Name the blood parasite species.
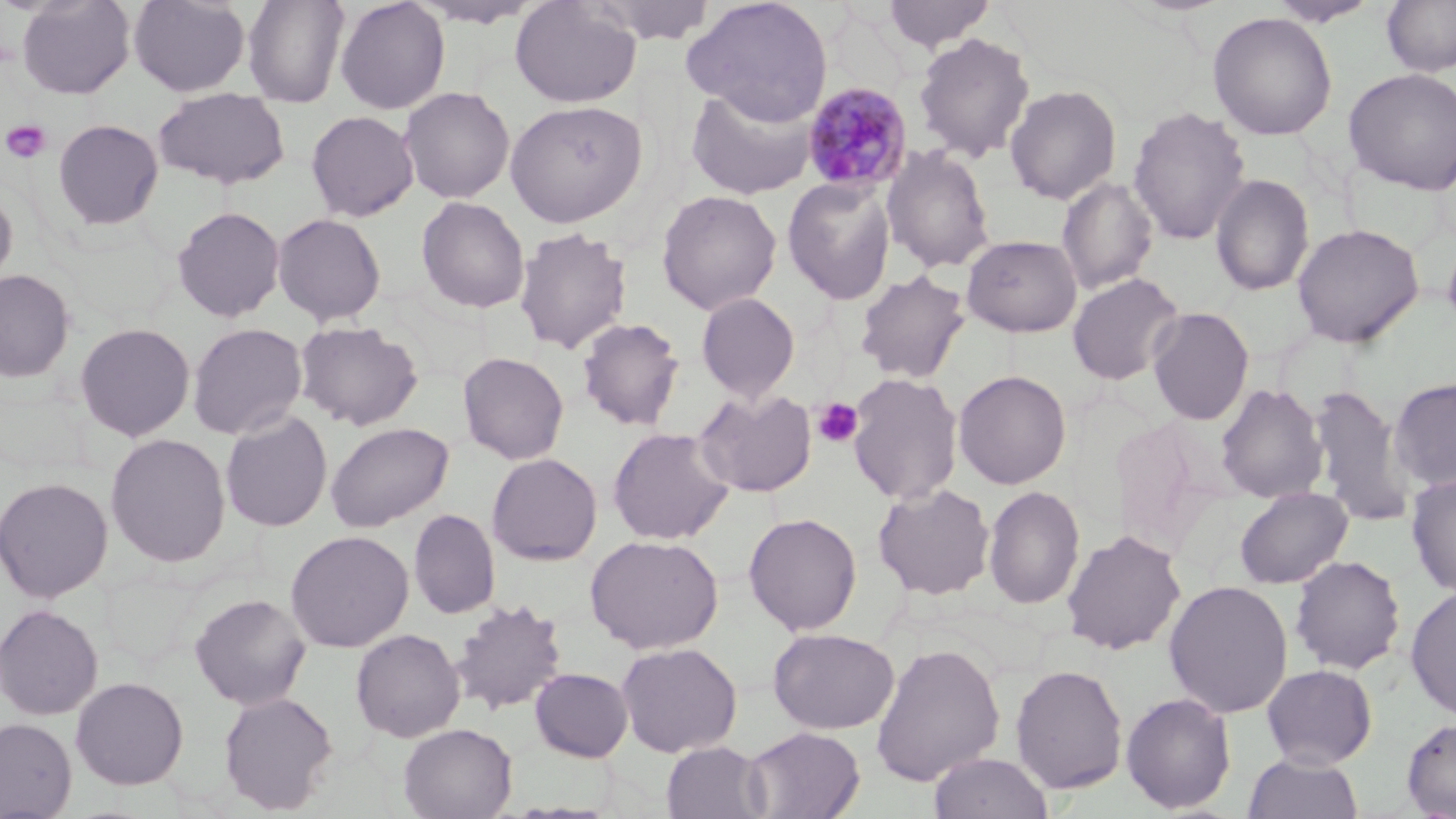
Plasmodium malariae.

modality = light microscopy
field of view = one of a larger specimen
magnification = 1000x
platelet locations = approximate bounding boxes as [x1, y1, x2, y2] in pixels: [2, 119, 52, 164], [812, 397, 864, 449]
preparation = thin blood film
image size = 1456×819 pixels
uninfected red blood cell locations = approximate bounding boxes as [x1, y1, x2, y2] in pixels: [16, 0, 136, 99], [129, 0, 250, 97], [242, 0, 351, 106], [335, 0, 450, 114], [409, 0, 544, 29], [585, 0, 719, 44], [683, 0, 833, 125], [882, 0, 995, 51], [1268, 0, 1381, 27], [510, 1, 642, 108], [1382, 1, 1456, 77], [1207, 11, 1338, 140], [914, 32, 1035, 163], [1344, 68, 1456, 195], [685, 83, 819, 200], [1004, 84, 1122, 204], [399, 86, 515, 204], [153, 88, 290, 189], [505, 99, 647, 227], [1128, 105, 1251, 246], [306, 111, 419, 222], [52, 119, 164, 230], [881, 143, 996, 274], [1210, 173, 1314, 296], [782, 177, 897, 304], [1057, 177, 1159, 295], [0, 184, 18, 291], [656, 189, 782, 315], [416, 196, 530, 314], [172, 206, 285, 322], [272, 213, 387, 326], [1291, 222, 1424, 348], [514, 226, 632, 355], [961, 235, 1083, 337], [0, 269, 76, 382], [855, 270, 970, 384], [1067, 273, 1185, 385], [696, 292, 801, 403], [1147, 307, 1254, 426], [576, 317, 685, 431], [294, 320, 424, 431], [74, 322, 195, 441], [187, 322, 308, 440], [458, 352, 569, 465], [471, 352, 584, 566], [953, 370, 1072, 489], [847, 373, 963, 506], [1389, 377, 1456, 491], [1216, 383, 1328, 504], [1308, 383, 1414, 527], [693, 387, 817, 497], [220, 410, 333, 532], [1109, 414, 1220, 558], [325, 421, 454, 532], [607, 427, 735, 545], [105, 433, 231, 567], [486, 453, 602, 565], [1406, 473, 1456, 598], [0, 477, 113, 603], [872, 482, 995, 601], [983, 485, 1085, 610], [1234, 486, 1353, 589], [409, 508, 500, 620], [744, 512, 862, 635], [1061, 529, 1186, 655], [285, 530, 413, 652], [585, 534, 724, 654], [1290, 554, 1406, 674], [1164, 580, 1294, 718], [1405, 585, 1456, 721], [189, 593, 311, 709], [449, 598, 568, 716], [0, 604, 104, 720], [350, 628, 465, 742], [768, 628, 899, 734], [616, 641, 743, 757], [870, 641, 1005, 787], [1010, 663, 1128, 794], [1261, 664, 1378, 769], [529, 667, 633, 762], [70, 676, 189, 789], [217, 690, 339, 814], [1121, 692, 1237, 813], [0, 717, 77, 818], [1401, 717, 1456, 818], [398, 723, 518, 819], [743, 726, 865, 818], [661, 741, 770, 819], [927, 751, 1054, 819], [1243, 752, 1363, 819]
stain = May-Grünwald-Giemsa
Plasmodium malariae-infected red blood cell locations = approximate bounding boxes as [x1, y1, x2, y2] in pixels: [802, 82, 913, 194]